Classify this cell by malaria status.
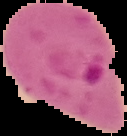

Parasitized.

Image is 127×136 pixels. From a thin blood smear. Cell region segmented out of the field of view; the surrounding area is masked to black.